Identify the parasite.
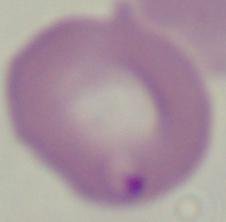

This is Babesia.

Summary:
  - Modality: micrograph
  - Magnification: 1000x